State the blood parasite species.
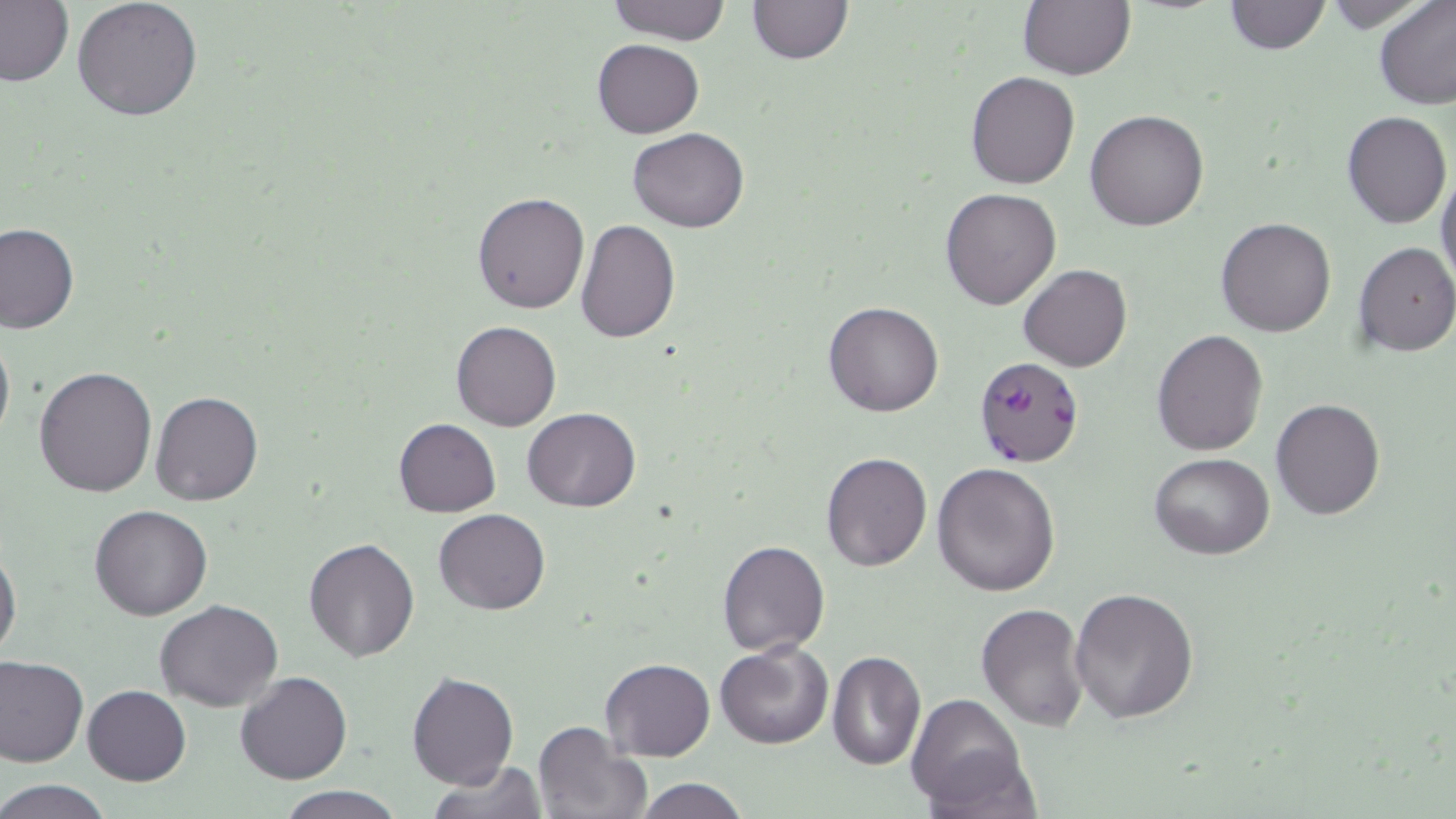
Plasmodium falciparum.

magnification = 1000x
field of view = one of a larger specimen
uninfected red blood cell locations = approximate bounding boxes as (x1, y1, x2, y2) in pixels: (71, 0, 204, 121), (605, 0, 732, 44), (747, 0, 852, 63), (1224, 0, 1329, 55), (1374, 0, 1456, 110), (1, 2, 71, 86), (1017, 2, 1135, 79), (592, 39, 704, 138), (966, 72, 1080, 189), (1084, 108, 1210, 230), (1341, 111, 1452, 228), (627, 128, 749, 232), (1435, 162, 1456, 291), (940, 187, 1062, 311), (472, 191, 590, 314), (1216, 217, 1336, 337), (575, 219, 679, 342), (1, 222, 77, 334), (1353, 242, 1456, 357), (1018, 263, 1132, 372), (823, 302, 944, 417), (451, 321, 561, 432), (0, 324, 14, 455), (1151, 329, 1269, 456), (32, 367, 159, 498), (150, 391, 263, 507), (1270, 397, 1388, 520), (521, 408, 641, 512), (394, 418, 500, 516), (821, 451, 933, 572), (1151, 454, 1275, 558), (932, 461, 1060, 597), (89, 504, 214, 621), (434, 508, 551, 615), (302, 536, 420, 662), (717, 539, 831, 656), (0, 544, 22, 664), (1070, 588, 1200, 725), (154, 601, 283, 712), (974, 603, 1091, 732), (714, 642, 834, 748), (827, 649, 925, 772), (0, 654, 88, 767), (599, 658, 716, 761), (406, 670, 519, 790), (235, 671, 352, 785), (81, 684, 191, 786), (907, 693, 1029, 811), (533, 719, 653, 819), (427, 760, 549, 819), (632, 777, 749, 819), (0, 779, 114, 818), (276, 785, 403, 819)
stain = May-Grünwald-Giemsa
modality = light microscopy
Plasmodium falciparum-infected red blood cell locations = approximate bounding boxes as (x1, y1, x2, y2) in pixels: (973, 357, 1086, 468)
image size = 1456×819 pixels
preparation = thin blood smear